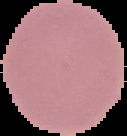

Summary:
  - Image type: cell region segmented out of the field of view; surrounding area masked to black
  - Result: no malaria parasites seen
  - Preparation: thin blood film
  - Image size: 127×136 pixels